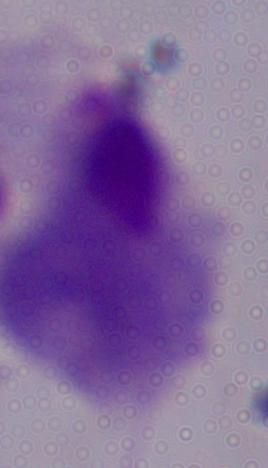

identification: trichomonad
modality: micrograph
magnification: 1000x